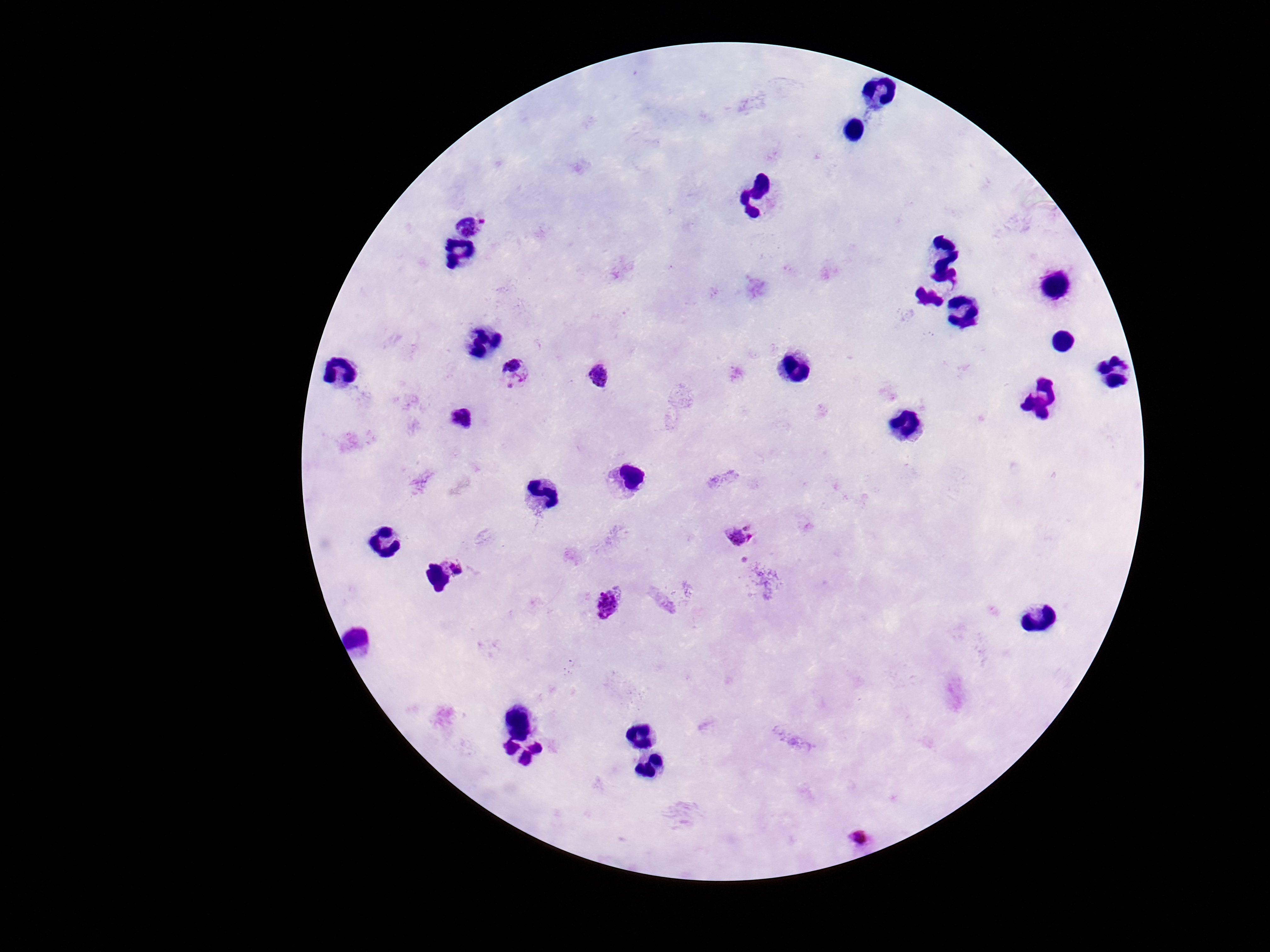

Approximate centers as (x, y) in pixels. Plasmodium parasite locations: (471, 223), (516, 373), (602, 377), (463, 419), (741, 536), (456, 564), (609, 603), (864, 840). Smartphone photograph taken through the microscope eyepiece. Thick blood smear. Image is 1270×952 pixels. Single field of view. 100x magnification. Patient malaria status: positive. Giemsa stain.